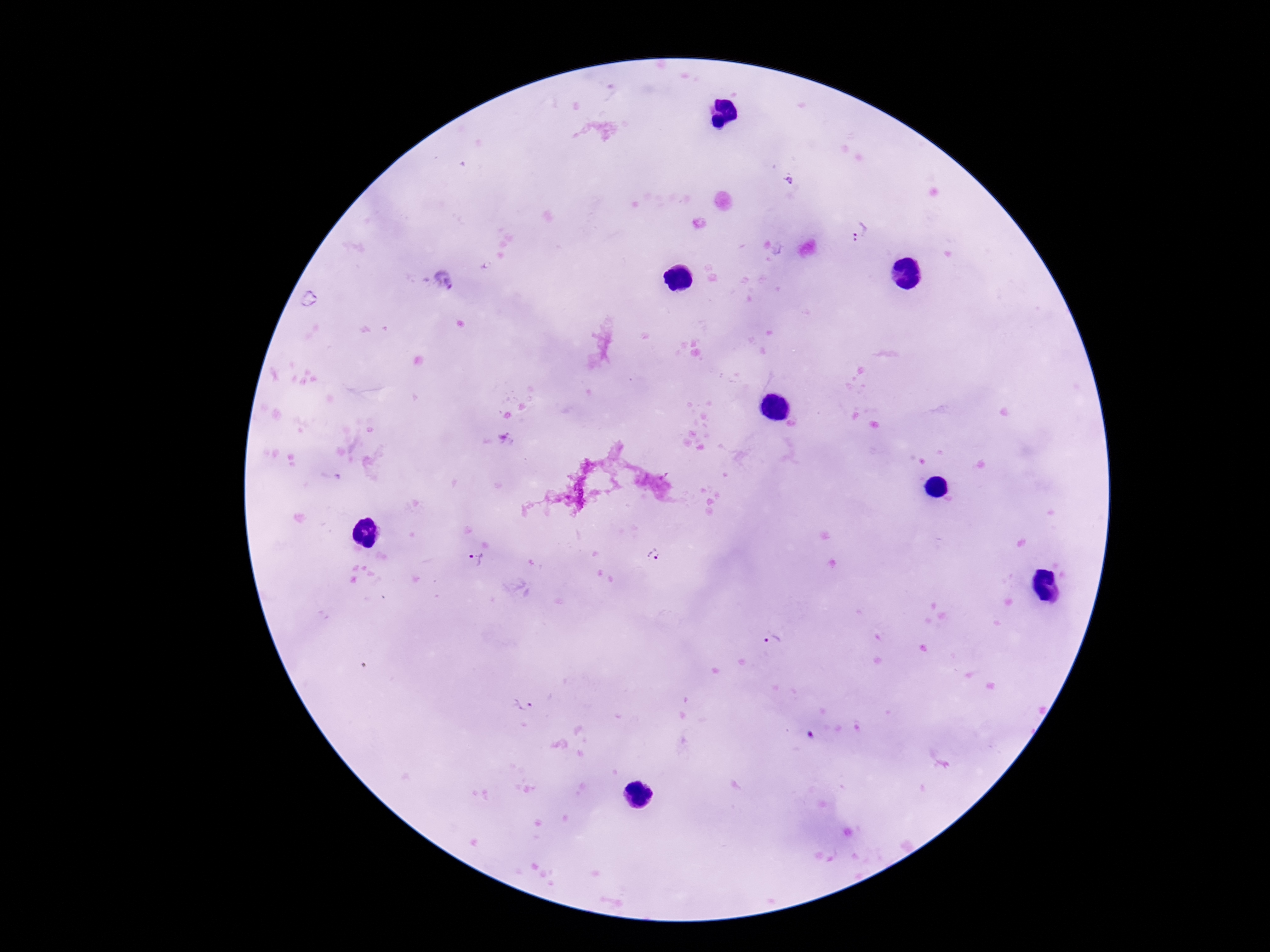 Approximate centers as [x, y] in pixels. Plasmodium parasite locations: [860, 233], [443, 280], [653, 557], [475, 559], [775, 641], [523, 708]. 100x magnification. Giemsa-stained preparation. Single field of view. Patient malaria status: infected. Thick blood smear. Photographed through the microscope eyepiece with a smartphone camera. Image is 1270×952 pixels.